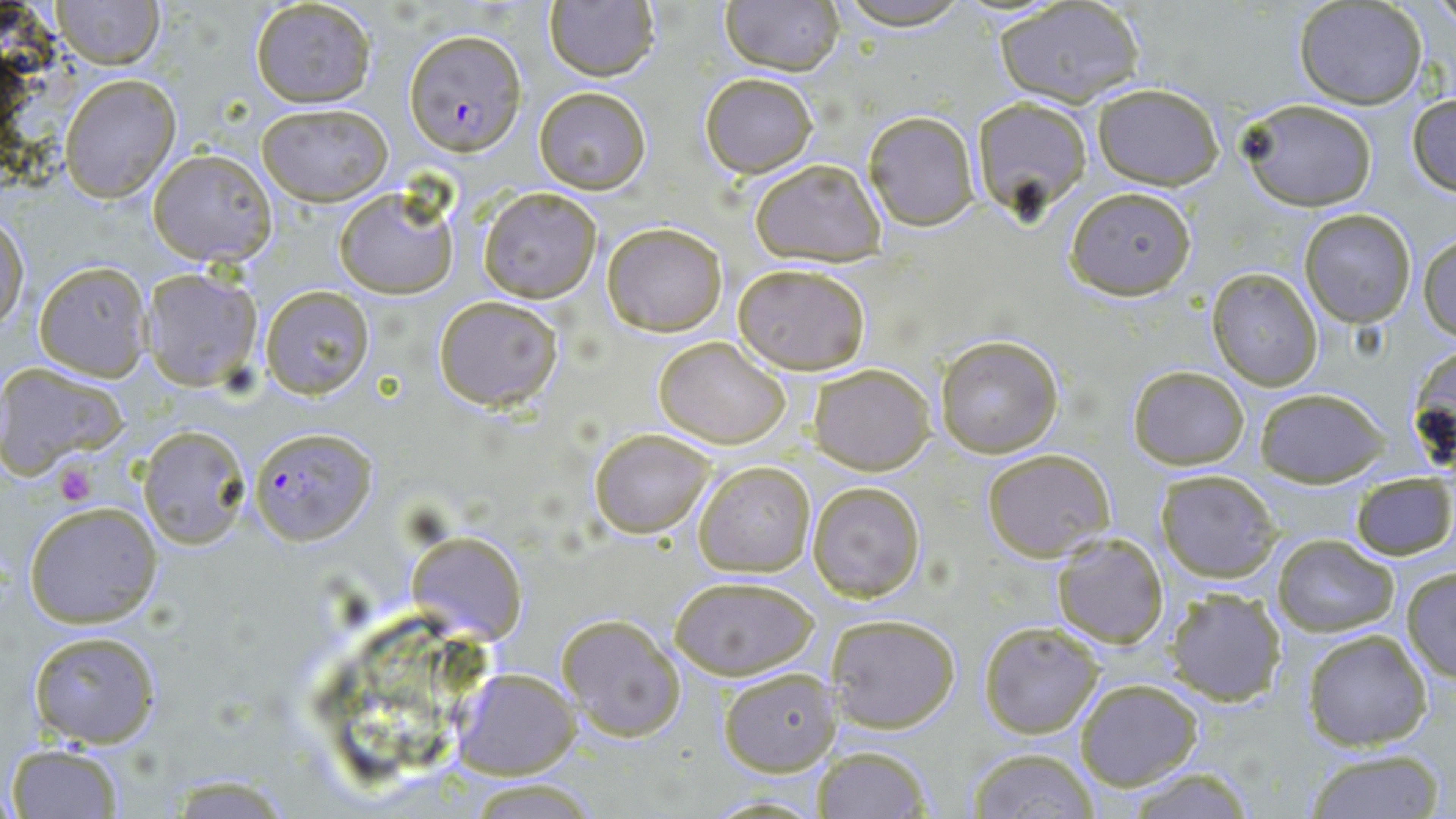

Summary:
  - Coordinate format: approximate bounding boxes as named x1/y1/x2/y2 corners in pixels
  - Plasmodium falciparum-infected red blood cell locations: (x1=402, y1=29, x2=525, y2=155), (x1=250, y1=425, x2=378, y2=545)
  - Uninfected red blood cell locations: (x1=50, y1=0, x2=164, y2=69), (x1=720, y1=0, x2=844, y2=75), (x1=249, y1=1, x2=377, y2=107), (x1=831, y1=1, x2=974, y2=29), (x1=543, y1=2, x2=659, y2=81), (x1=996, y1=2, x2=1146, y2=109), (x1=1295, y1=2, x2=1427, y2=109), (x1=700, y1=72, x2=818, y2=177), (x1=59, y1=74, x2=179, y2=202), (x1=1092, y1=82, x2=1224, y2=188), (x1=532, y1=87, x2=651, y2=194), (x1=1406, y1=91, x2=1455, y2=195), (x1=971, y1=96, x2=1092, y2=215), (x1=1239, y1=96, x2=1380, y2=211), (x1=256, y1=103, x2=392, y2=205), (x1=861, y1=109, x2=980, y2=230), (x1=147, y1=148, x2=276, y2=266), (x1=750, y1=159, x2=887, y2=266), (x1=334, y1=183, x2=460, y2=300), (x1=1065, y1=185, x2=1196, y2=299), (x1=477, y1=187, x2=602, y2=303), (x1=1299, y1=208, x2=1416, y2=327), (x1=0, y1=215, x2=29, y2=334), (x1=600, y1=221, x2=727, y2=335), (x1=1419, y1=233, x2=1455, y2=341), (x1=35, y1=261, x2=152, y2=379), (x1=733, y1=262, x2=870, y2=375), (x1=142, y1=269, x2=265, y2=390), (x1=1206, y1=269, x2=1322, y2=390), (x1=261, y1=284, x2=374, y2=398), (x1=433, y1=294, x2=563, y2=411), (x1=935, y1=334, x2=1065, y2=459), (x1=652, y1=336, x2=791, y2=450), (x1=1406, y1=341, x2=1454, y2=478), (x1=0, y1=364, x2=129, y2=474), (x1=811, y1=364, x2=934, y2=475), (x1=1127, y1=364, x2=1251, y2=471), (x1=1253, y1=386, x2=1388, y2=486), (x1=138, y1=426, x2=248, y2=546), (x1=590, y1=429, x2=712, y2=536), (x1=982, y1=448, x2=1116, y2=561), (x1=694, y1=459, x2=816, y2=576), (x1=1155, y1=470, x2=1282, y2=582), (x1=1350, y1=473, x2=1455, y2=560), (x1=809, y1=480, x2=925, y2=601), (x1=23, y1=499, x2=164, y2=627), (x1=407, y1=531, x2=526, y2=645), (x1=1051, y1=532, x2=1169, y2=649), (x1=1271, y1=535, x2=1398, y2=637), (x1=1402, y1=566, x2=1455, y2=681), (x1=668, y1=575, x2=820, y2=679), (x1=1163, y1=588, x2=1285, y2=707), (x1=557, y1=613, x2=685, y2=743), (x1=828, y1=613, x2=960, y2=733), (x1=978, y1=620, x2=1104, y2=739), (x1=1303, y1=629, x2=1433, y2=751), (x1=27, y1=630, x2=162, y2=747), (x1=454, y1=668, x2=580, y2=780), (x1=719, y1=668, x2=838, y2=776), (x1=1074, y1=678, x2=1203, y2=788), (x1=6, y1=743, x2=125, y2=817), (x1=811, y1=745, x2=934, y2=818), (x1=968, y1=748, x2=1100, y2=818), (x1=1302, y1=748, x2=1445, y2=819), (x1=1118, y1=768, x2=1257, y2=818), (x1=163, y1=777, x2=296, y2=816), (x1=465, y1=780, x2=600, y2=817), (x1=701, y1=793, x2=829, y2=817)
  - Platelet locations: (x1=56, y1=464, x2=97, y2=505)
  - Slide-level diagnosis: Plasmodium falciparum
  - Field of view: one of a larger specimen
  - Image size: 1456×819 pixels
  - Modality: optical microscopy
  - Stain: May-Grünwald-Giemsa
  - Magnification: 1000x
  - Preparation: thin blood film